Classify this cell by malaria status.
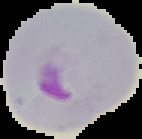

It is parasitized.

image size = 142×139 pixels
image type = cell region segmented out of the field of view; surrounding area masked to black
preparation = thin blood film